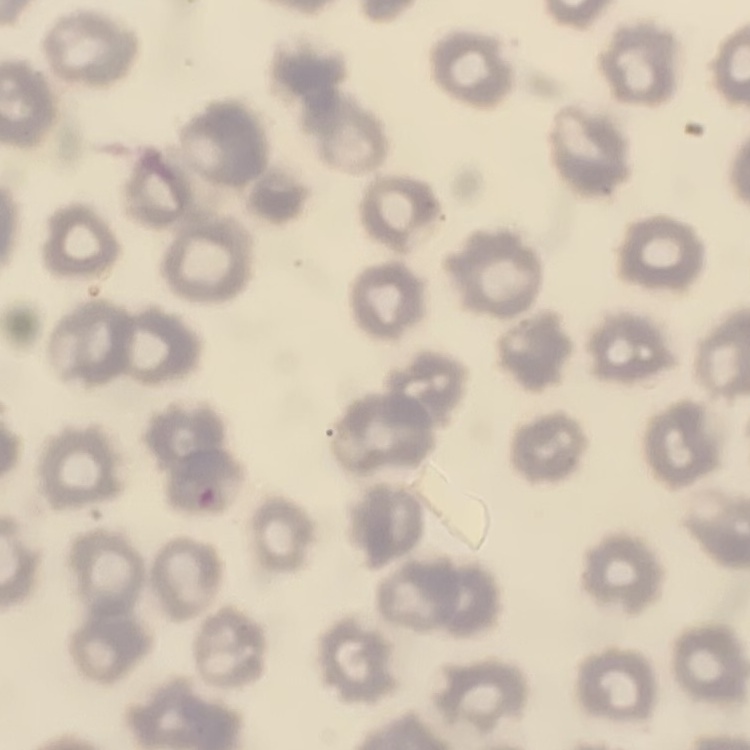
erythrocyte morphology = no rouleaux formation
preparation = thin blood smear
stain = Field's or Giemsa
image type = square crop of a larger photomicrograph